Evaluate for parasitized red blood cells.
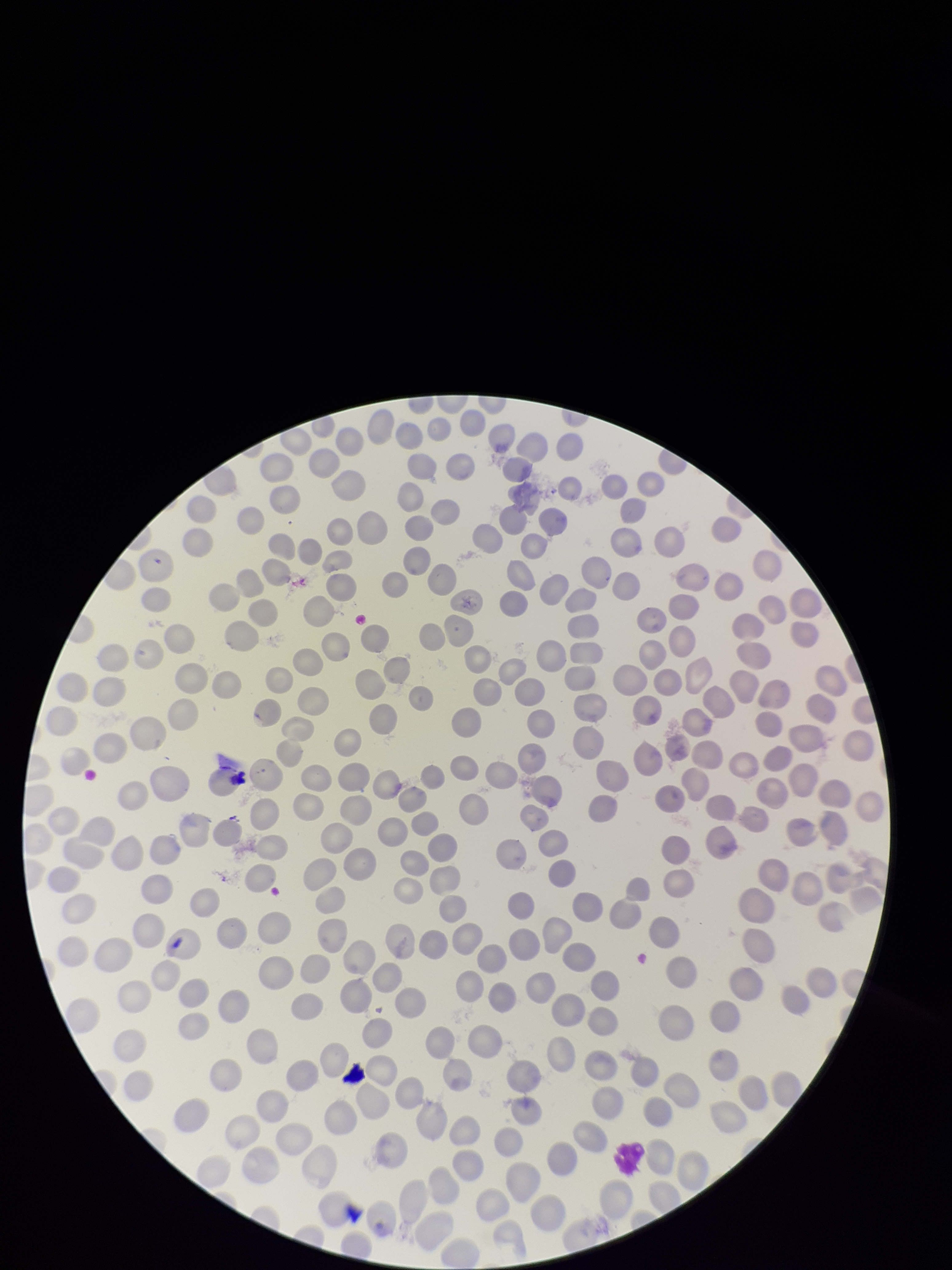

None detected.

stain = Giemsa
capture = smartphone photograph through the microscope eyepiece
field of view = single
species reported for this patient = Plasmodium falciparum
patient malaria status = positive
red blood cell count = 261
image size = 952×1270 pixels
preparation = thin blood smear
parasitized red blood cell count = 0